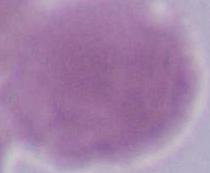
Summary:
  - Modality: photomicrograph
  - Magnification: 1000x
  - Identification: erythrocyte